Assess this cell for malaria.
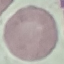
It is uninfected.

Thin blood smear. Photographed with a smartphone camera at the microscope eyepiece. Cell patch, automatically extracted from a larger field of view and resized to 64 × 64 pixels. Giemsa-stained preparation.